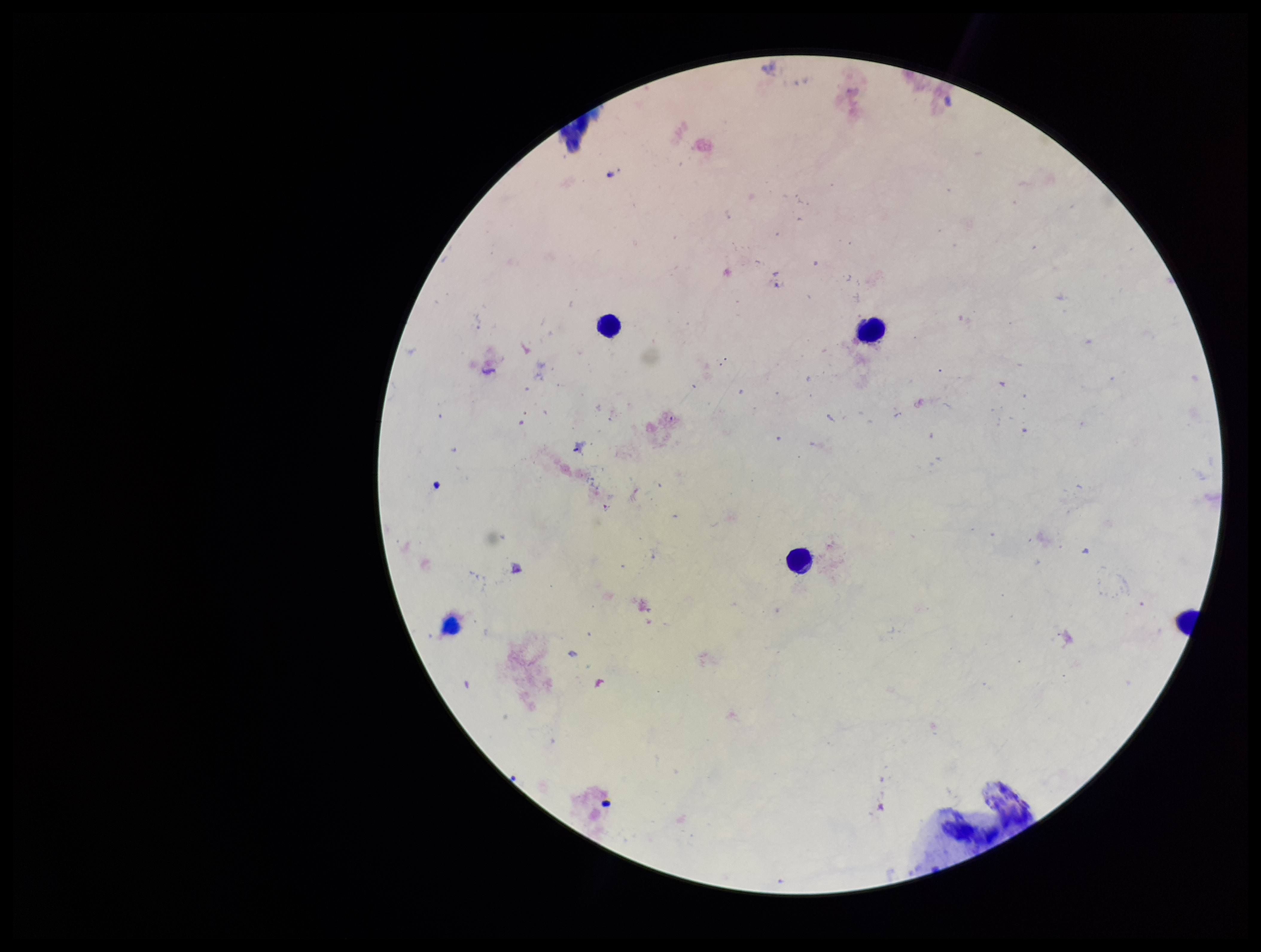

Summary:
  - Patient malaria status: negative
  - Capture: smartphone photograph through the microscope eyepiece
  - Leukocyte count: 4
  - Image size: 1261×952 pixels
  - Stain: Giemsa
  - Field of view: one from this slide
  - Plasmodium parasites: none detected
  - Preparation: thick
  - Parasite count: 0